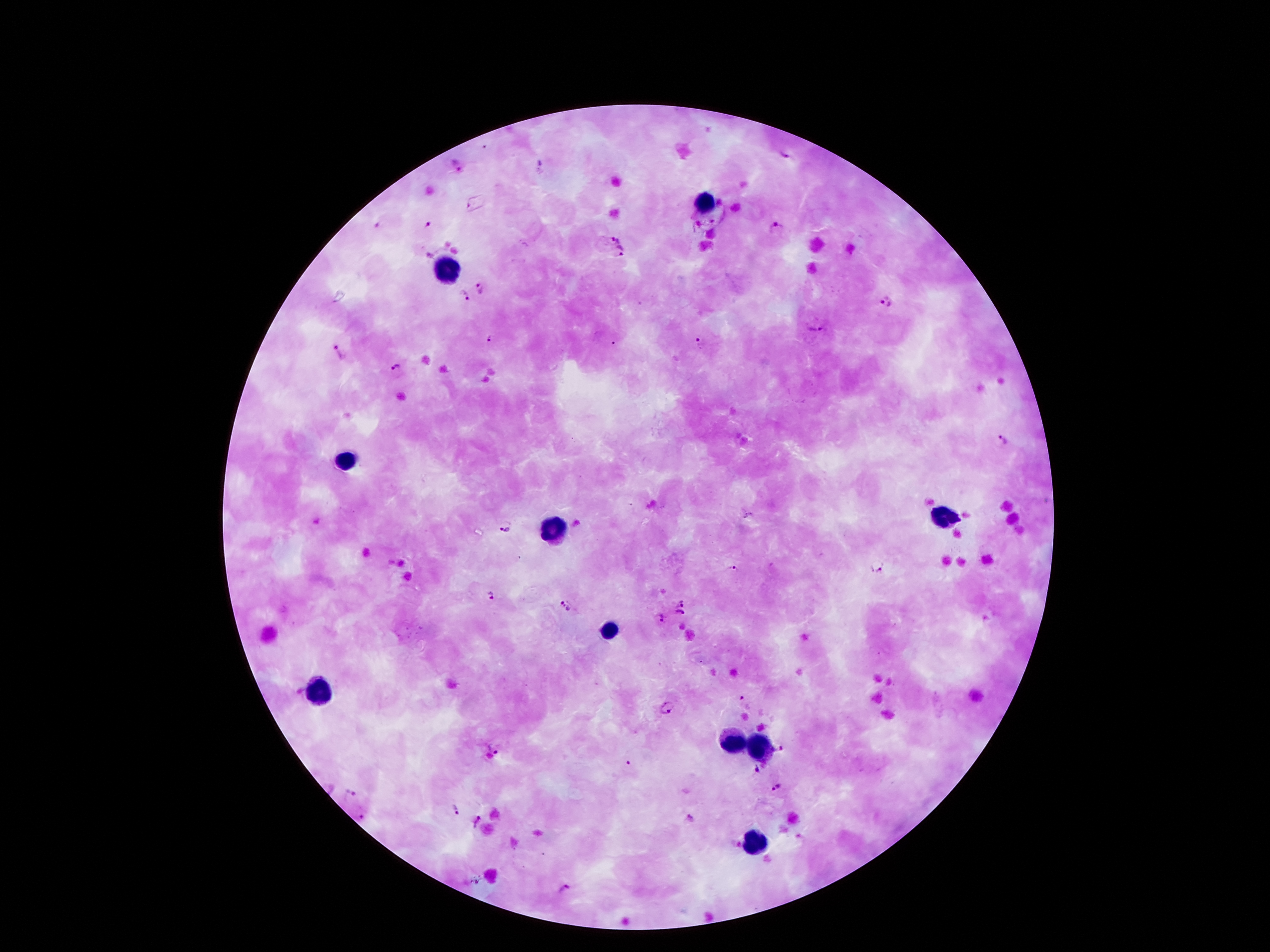

One field from this slide. Thick blood smear. Patient malaria status: positive for Plasmodium falciparum. Giemsa stain. Photographed through the microscope eyepiece with a smartphone camera. Image is 1270×952 pixels. 100x magnification.